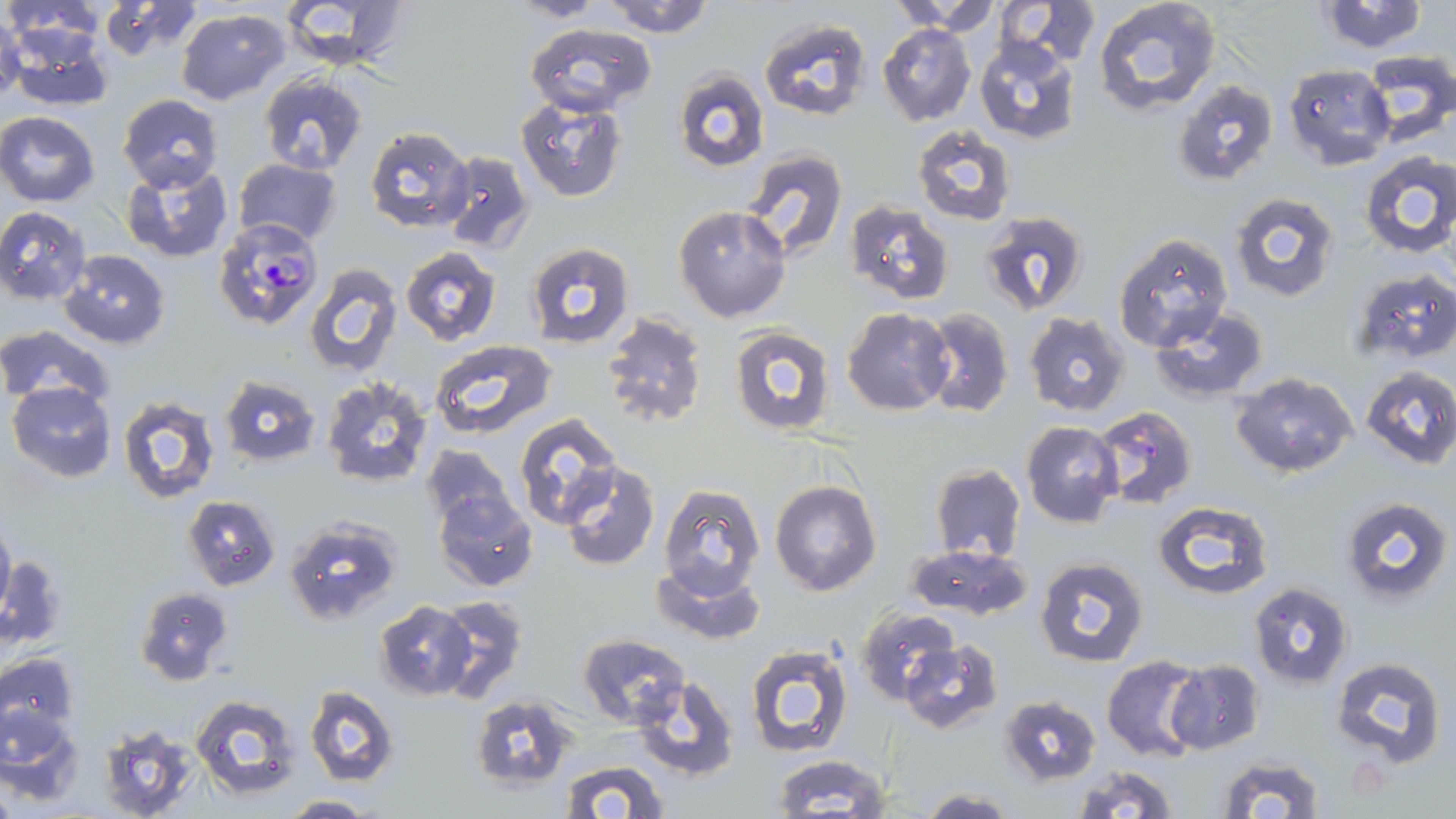
slide-level diagnosis = Plasmodium falciparum
stain = May-Grünwald-Giemsa
magnification = 1000x
uninfected red blood cell locations = approximate bounding boxes as (x1, y1, x2, y2) in pixels: (2, 0, 103, 44), (281, 0, 411, 73), (508, 0, 606, 22), (600, 0, 714, 37), (887, 0, 998, 31), (993, 0, 1103, 69), (1092, 0, 1221, 114), (1313, 0, 1433, 54), (98, 1, 201, 60), (175, 7, 289, 106), (0, 13, 25, 106), (759, 17, 870, 124), (525, 22, 656, 116), (877, 22, 976, 127), (4, 25, 115, 113), (973, 36, 1081, 144), (1359, 51, 1455, 147), (1281, 64, 1393, 169), (673, 71, 769, 172), (259, 74, 369, 175), (1172, 79, 1278, 187), (117, 92, 223, 190), (516, 99, 626, 202), (0, 111, 100, 206), (912, 125, 1017, 226), (365, 127, 476, 233), (738, 149, 850, 267), (1357, 150, 1456, 258), (440, 151, 535, 255), (232, 160, 342, 248), (121, 161, 234, 264), (1229, 193, 1341, 305), (845, 202, 952, 306), (674, 205, 791, 323), (0, 206, 92, 305), (980, 212, 1089, 314), (1114, 233, 1232, 351), (524, 242, 637, 350), (400, 247, 502, 345), (62, 250, 170, 349), (303, 264, 403, 378), (1352, 269, 1456, 364), (842, 307, 953, 415), (1149, 307, 1269, 401), (920, 308, 1014, 419), (1024, 311, 1131, 417), (600, 313, 708, 429), (0, 324, 115, 410), (729, 326, 837, 438), (430, 338, 558, 440), (1360, 365, 1456, 470), (1231, 371, 1358, 478), (220, 374, 321, 468), (320, 377, 434, 489), (6, 382, 116, 482), (116, 396, 220, 504), (1090, 404, 1199, 514), (513, 414, 624, 531), (1021, 421, 1124, 528), (421, 443, 514, 529), (560, 461, 661, 571), (929, 462, 1026, 564), (770, 480, 882, 596), (658, 484, 765, 600), (433, 488, 538, 592), (183, 494, 280, 591), (1339, 496, 1452, 605), (1153, 500, 1274, 599), (284, 516, 402, 625), (0, 518, 14, 620), (906, 544, 1033, 621), (3, 553, 66, 651), (1035, 556, 1148, 668), (651, 562, 765, 645), (1248, 581, 1354, 688), (135, 585, 234, 687), (433, 594, 527, 703), (374, 601, 476, 699), (858, 607, 960, 705), (579, 633, 690, 729), (899, 640, 1003, 734), (745, 643, 854, 758), (0, 652, 79, 736), (1101, 655, 1206, 762), (1330, 655, 1446, 768), (1166, 660, 1264, 754), (631, 677, 740, 780), (305, 687, 398, 786), (190, 694, 300, 799), (470, 694, 576, 791), (999, 694, 1102, 786), (1, 705, 85, 801), (98, 724, 201, 819), (771, 754, 892, 816), (1216, 754, 1325, 818), (560, 759, 669, 818), (1072, 763, 1181, 818), (917, 788, 1018, 818), (282, 793, 373, 817)
modality = light microscopy
preparation = thin blood film
Plasmodium falciparum-infected red blood cell locations = approximate bounding boxes as (x1, y1, x2, y2) in pixels: (213, 221, 323, 330)
image size = 1456×819 pixels
field of view = one of a larger specimen